Describe the morphology of the erythrocytes.
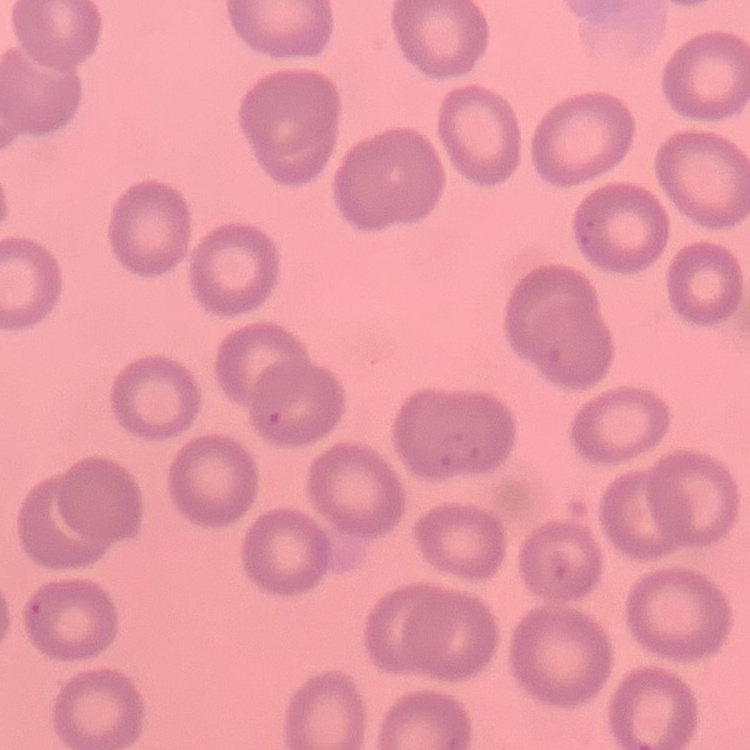
They show no rouleaux formation.

{
  "stain": "Field's or Giemsa",
  "preparation": "thin peripheral smear",
  "image_type": "square crop of a larger photomicrograph"
}